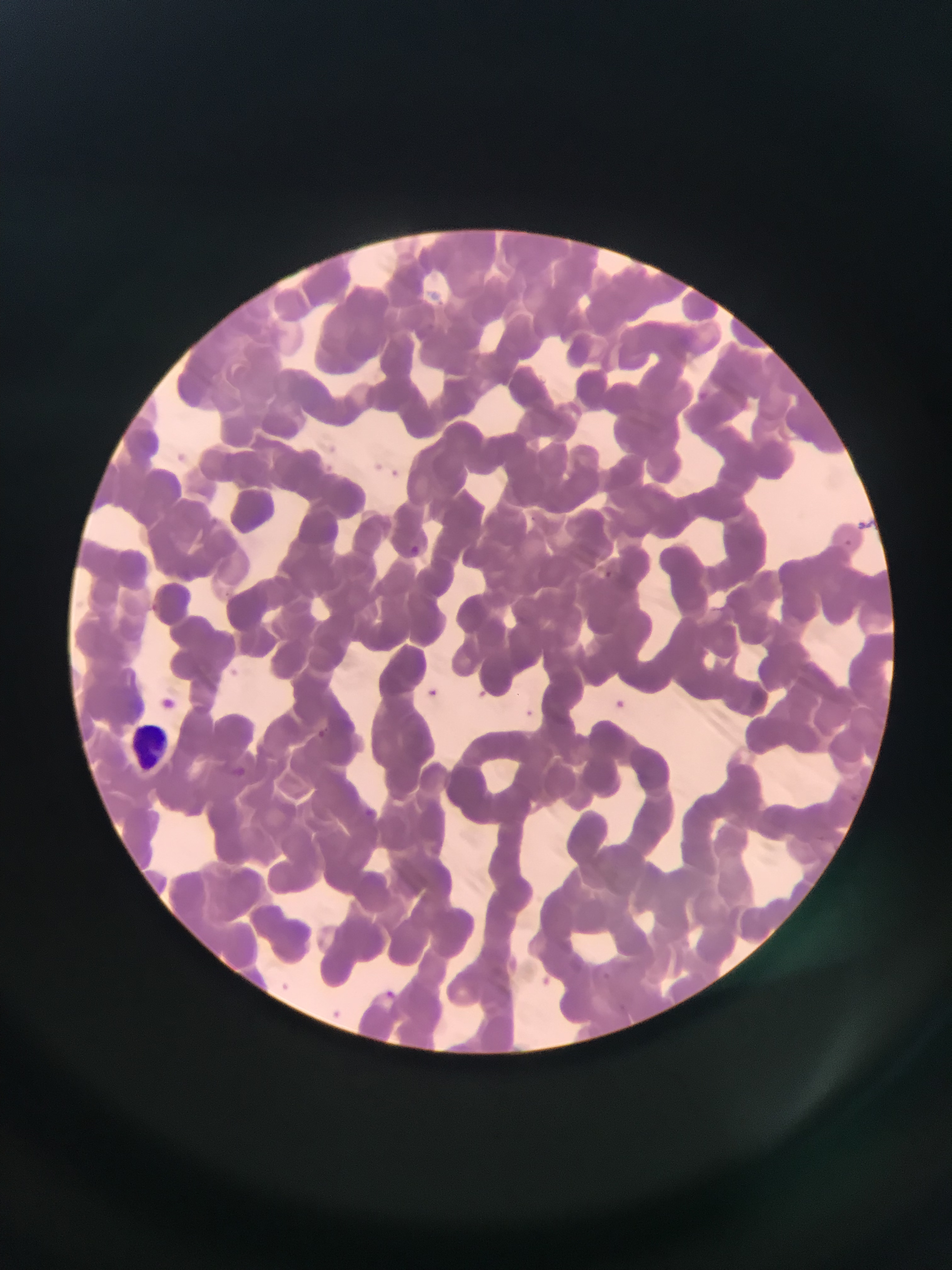
Approximate bounding boxes as (left, top, right, bottom) in pixels. Leukocyte locations: (125, 712, 176, 776). Plasmodium parasite locations: (696, 389, 711, 403), (372, 457, 385, 474), (390, 465, 411, 477), (526, 511, 541, 524), (857, 517, 881, 537), (838, 536, 850, 562), (407, 540, 422, 565), (601, 568, 613, 579), (423, 685, 441, 701), (161, 690, 180, 713), (606, 694, 629, 715), (517, 704, 540, 724), (314, 726, 335, 742), (227, 763, 248, 787), (358, 802, 375, 820), (380, 986, 399, 1004). Collected in Ghana. Image is 952×1270 pixels. Mobile-phone photograph taken through the microscope. Single field of view. Thin blood smear.